Locate every blood parasite and identify its species.
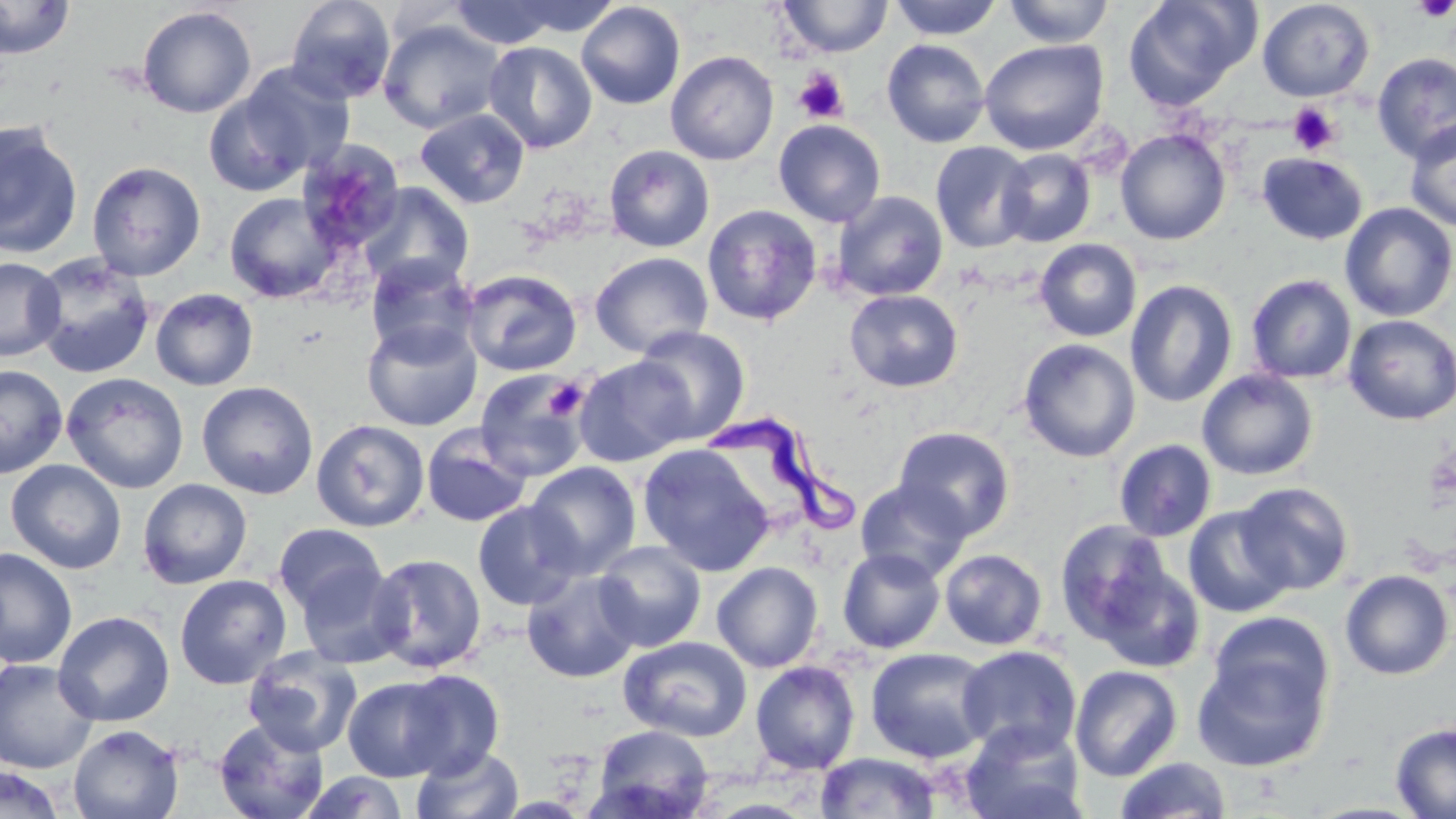

Approximate bounding boxes as (x1, y1, x2, y2) in pixels.
Trypanosoma brucei: (704, 411, 863, 537).
No Plasmodium falciparum, Plasmodium ovale, Plasmodium malariae, Plasmodium vivax, or Babesia divergens observed.

Platelet locations: (1411, 0, 1455, 22), (793, 69, 849, 124), (1287, 102, 1340, 154), (543, 377, 588, 421). Uninfected red blood cell locations: (0, 0, 76, 60), (285, 0, 396, 104), (508, 0, 621, 37), (778, 0, 893, 58), (888, 0, 1003, 39), (1002, 0, 1115, 47), (1122, 0, 1258, 109), (1257, 0, 1375, 102), (449, 1, 564, 49), (576, 2, 686, 109), (137, 6, 256, 118), (378, 19, 507, 134), (881, 39, 990, 148), (979, 39, 1109, 155), (483, 41, 597, 153), (665, 51, 779, 165), (1372, 53, 1456, 164), (229, 63, 356, 181), (202, 87, 316, 197), (415, 108, 530, 208), (1404, 118, 1456, 232), (773, 119, 886, 227), (0, 121, 83, 259), (1115, 128, 1231, 245), (295, 139, 405, 256), (931, 142, 1036, 253), (604, 144, 715, 252), (997, 148, 1095, 246), (1257, 152, 1368, 244), (86, 160, 207, 280), (357, 183, 473, 293), (831, 190, 948, 301), (224, 192, 341, 303), (1339, 202, 1456, 322), (702, 205, 822, 325), (1034, 238, 1142, 342), (590, 251, 713, 358), (30, 253, 157, 377), (365, 255, 480, 363), (0, 256, 65, 361), (461, 268, 582, 377), (1246, 274, 1357, 384), (1125, 279, 1238, 408), (150, 288, 258, 390), (844, 289, 963, 392), (1343, 314, 1456, 425), (362, 319, 482, 431), (632, 325, 751, 443), (1018, 339, 1140, 462), (573, 355, 695, 468), (0, 364, 67, 478), (474, 368, 592, 482), (1197, 369, 1318, 481), (62, 372, 189, 494), (197, 380, 319, 499), (311, 419, 429, 532), (421, 426, 532, 529), (893, 426, 1015, 540), (1114, 439, 1217, 542), (638, 443, 776, 577), (5, 459, 127, 574), (525, 462, 640, 578), (137, 478, 253, 589), (855, 480, 971, 582), (1233, 481, 1354, 596), (472, 501, 583, 610), (1182, 505, 1297, 619), (1055, 519, 1176, 643), (273, 523, 386, 617), (593, 541, 706, 652), (0, 547, 77, 669), (837, 548, 946, 654), (939, 549, 1047, 650), (368, 553, 486, 673), (295, 561, 408, 669), (1092, 561, 1206, 673), (712, 562, 824, 673), (522, 568, 642, 683), (1339, 569, 1454, 680), (174, 574, 292, 689), (53, 611, 174, 727), (1207, 612, 1334, 722), (619, 635, 752, 742), (956, 644, 1083, 759), (243, 646, 363, 757), (865, 647, 994, 764), (1191, 647, 1332, 773), (0, 659, 98, 774), (750, 661, 860, 774), (1070, 665, 1182, 781), (399, 669, 505, 779), (343, 677, 454, 782), (213, 718, 330, 819), (960, 722, 1088, 819), (1390, 723, 1456, 818), (68, 724, 183, 819), (592, 724, 714, 818), (412, 745, 524, 819), (815, 752, 942, 818), (1114, 757, 1231, 818), (1, 765, 67, 819), (299, 771, 409, 818). Slide-level diagnosis: Trypanosoma brucei. One field of a larger specimen. May-Grünwald-Giemsa stain. Thin blood smear. Light microscopy. Image is 1456×819 pixels. Captured at 1000x magnification.